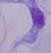 A trypanosome is shown. Micrograph. Captured at 1000x magnification.